Identify the parasite.
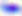
Toxoplasma gondii.

Summary:
  - Modality: photomicrograph
  - Magnification: 400x